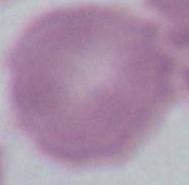

Summary:
  - Modality: photomicrograph
  - Identification: red blood cell
  - Magnification: 1000x